Point out each Plasmodium parasite.
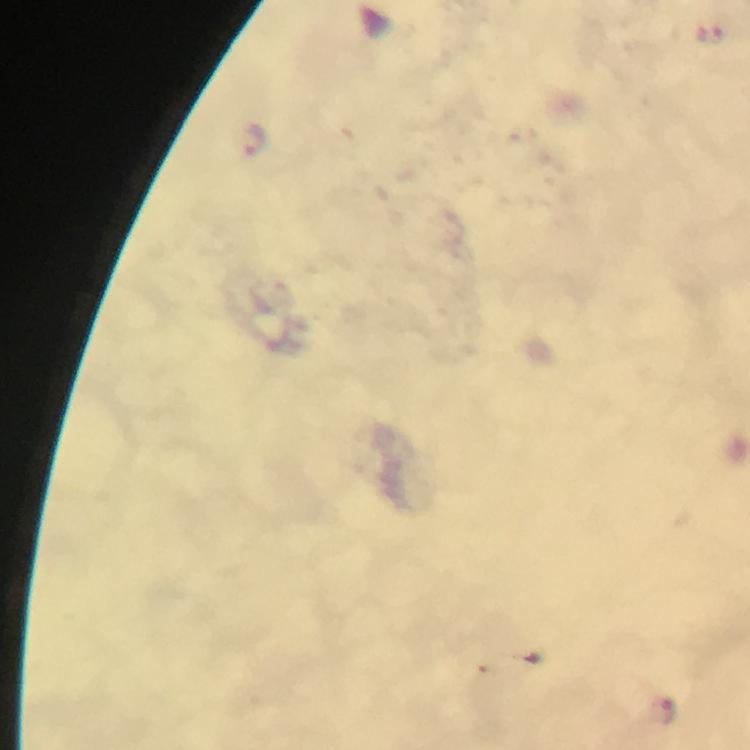
Approximate centers as {x, y} in pixels.
Plasmodium parasites: {253, 140}, {667, 710}.

Summary:
  - Capture: smartphone photograph through a microscope
  - Magnification: 100x
  - Context: from a malaria diagnostic workup
  - Stain: Giemsa
  - Immersion oil: used
  - Preparation: thick blood film
  - Image size: 750×750 pixels
  - Cropped from: a single field of view